Identify the blood parasite species.
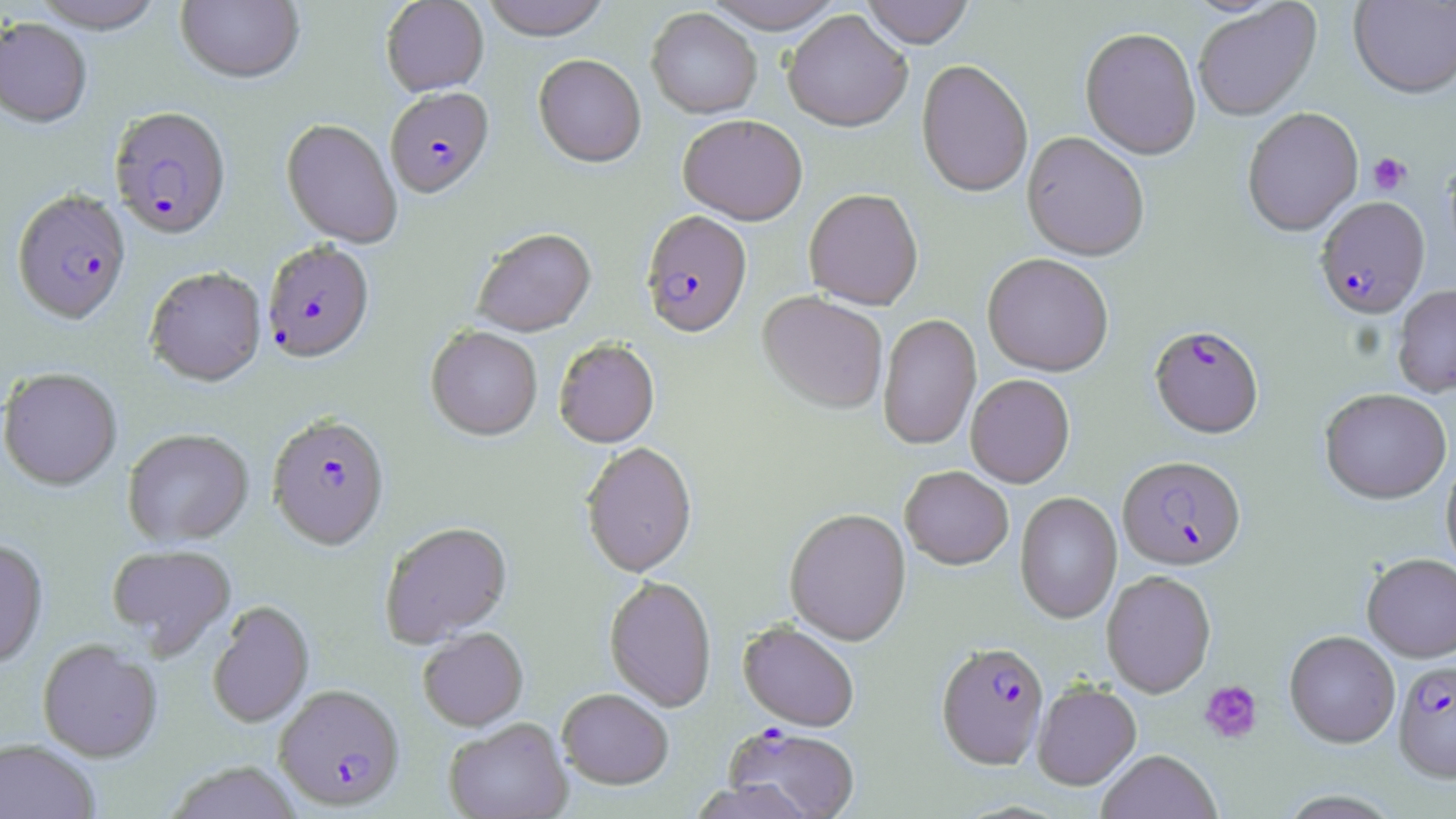
Plasmodium falciparum.

Summary:
  - Coordinate format: approximate bounding boxes as (x1,y1)-(x2,y2) corner pairs in pixels
  - Plasmodium falciparum-infected red blood cell locations: (386,90)-(495,201), (108,109)-(232,243), (12,192)-(131,328), (1315,198)-(1430,321), (640,213)-(753,341), (262,243)-(375,366), (1149,327)-(1264,441), (267,417)-(389,553), (1117,458)-(1246,572), (935,643)-(1049,771), (1394,661)-(1456,786), (274,686)-(405,811), (724,725)-(860,819)
  - Uninfected red blood cell locations: (30,0)-(165,36), (175,0)-(305,87), (381,0)-(489,97), (481,0)-(612,42), (702,0)-(846,35), (860,0)-(975,50), (1349,0)-(1456,100), (1193,3)-(1322,122), (646,8)-(762,120), (782,11)-(912,133), (0,20)-(92,131), (1079,29)-(1201,163), (533,55)-(646,170), (916,60)-(1033,201), (1242,108)-(1363,238), (678,117)-(808,227), (280,120)-(402,251), (1021,133)-(1149,263), (803,190)-(924,311), (472,230)-(597,338), (982,255)-(1114,378), (145,270)-(267,389), (1392,285)-(1456,399), (757,293)-(888,415), (878,313)-(981,451), (426,327)-(542,443), (554,341)-(660,449), (1,369)-(122,492), (965,375)-(1075,489), (1319,389)-(1451,507), (123,430)-(254,548), (581,443)-(697,580), (1440,458)-(1456,579), (899,467)-(1013,571), (1014,492)-(1122,625), (784,509)-(912,647), (380,523)-(513,648), (0,540)-(49,671), (107,545)-(236,657), (1361,555)-(1456,664), (1101,571)-(1216,698), (604,577)-(716,713), (207,602)-(315,729), (738,622)-(859,732), (418,629)-(529,732), (1284,632)-(1400,749), (38,641)-(163,763), (1032,683)-(1142,792), (557,689)-(673,791), (444,718)-(573,819), (0,739)-(99,819), (1096,751)-(1221,819), (164,762)-(302,818), (687,780)-(817,819)
  - Platelet locations: (1368,153)-(1412,195), (1199,680)-(1263,745)
  - Preparation: thin blood smear
  - Field of view: single
  - Stain: May-Grünwald-Giemsa
  - Image size: 1456×819 pixels
  - Magnification: 1000x
  - Modality: optical microscopy